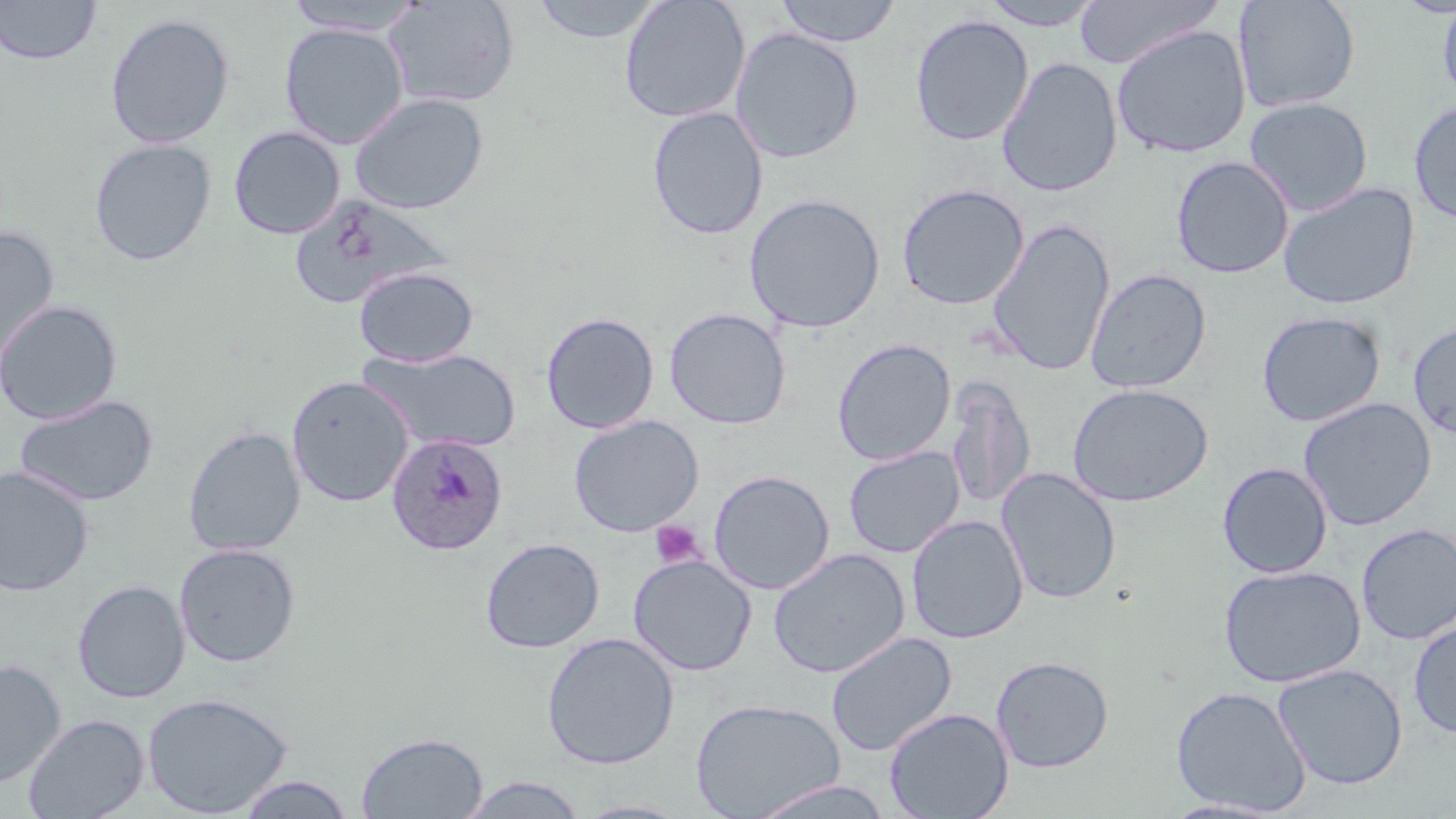
{
  "slide_level_diagnosis": "Plasmodium ovale",
  "stain": "May-Grünwald-Giemsa",
  "plasmodium_ovale_infected_red_blood_cell_locations": "approximate bounding boxes as [x1, y1, x2, y2] in pixels: [386, 433, 508, 556]",
  "image_size": "1456×819 pixels",
  "preparation": "thin blood film",
  "modality": "optical microscopy",
  "uninfected_red_blood_cell_locations": "approximate bounding boxes as [x1, y1, x2, y2] in pixels: [0, 0, 101, 65], [531, 0, 665, 44], [773, 0, 902, 47], [978, 0, 1105, 30], [1073, 0, 1222, 70], [1233, 0, 1361, 113], [282, 1, 428, 35], [382, 1, 519, 109], [619, 1, 750, 123], [1437, 1, 1456, 107], [105, 13, 235, 149], [910, 14, 1033, 146], [279, 23, 408, 149], [1111, 25, 1251, 158], [730, 28, 864, 163], [997, 57, 1123, 198], [349, 92, 489, 215], [1244, 97, 1374, 216], [1408, 100, 1456, 226], [646, 106, 768, 240], [229, 126, 344, 239], [89, 138, 216, 266], [1171, 156, 1294, 279], [1278, 182, 1420, 310], [897, 183, 1029, 310], [743, 193, 885, 333], [289, 194, 454, 310], [986, 219, 1115, 377], [0, 226, 61, 367], [353, 266, 480, 367], [1084, 268, 1212, 394], [0, 299, 122, 424], [664, 307, 791, 429], [1256, 311, 1386, 427], [541, 312, 659, 434], [1407, 320, 1456, 441], [832, 338, 956, 466], [358, 348, 521, 453], [286, 375, 414, 507], [945, 379, 1035, 512], [1067, 383, 1213, 506], [14, 394, 158, 507], [1298, 397, 1436, 531], [568, 415, 704, 537], [183, 426, 305, 557], [843, 446, 965, 558], [1217, 462, 1333, 578], [0, 466, 95, 596], [996, 467, 1121, 605], [708, 469, 835, 595], [906, 515, 1028, 644], [1356, 523, 1456, 645], [480, 537, 604, 654], [174, 543, 301, 667], [768, 548, 910, 679], [628, 554, 757, 676], [1218, 564, 1365, 688], [73, 580, 189, 703], [1408, 618, 1456, 740], [541, 632, 679, 770], [826, 632, 957, 757], [990, 655, 1114, 773], [0, 659, 66, 789], [1272, 663, 1408, 790], [1170, 685, 1312, 816], [142, 691, 293, 817], [690, 697, 844, 818], [884, 707, 1014, 818], [23, 713, 148, 819], [356, 731, 487, 819], [234, 774, 355, 818], [458, 774, 588, 818], [745, 779, 896, 819], [1160, 798, 1290, 818], [571, 799, 693, 818]",
  "field_of_view": "single",
  "platelet_locations": "approximate bounding boxes as [x1, y1, x2, y2] in pixels: [649, 520, 707, 569]",
  "magnification": "1000x"
}